Identify the cell.
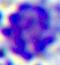

A leukocyte.

modality = photomicrograph
magnification = 400x